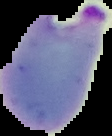
Cell region segmented out of the field of view; the surrounding area is masked to black. Malaria status: parasitized. Image is 112×136 pixels. From a thin blood smear.